Report the malaria status of this cell.
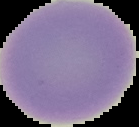

It is uninfected.

Segmented cell region on a black background. Image is 139×127 pixels. From a thin blood film.